State which parasite is depicted.
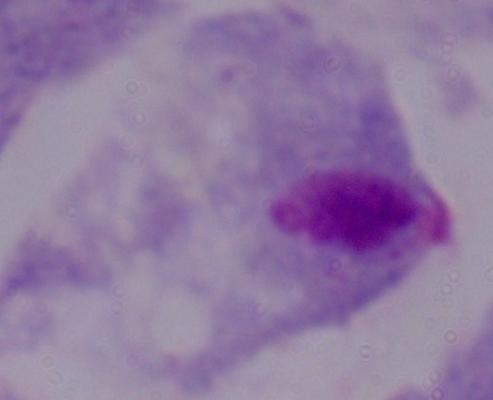

A trichomonad.

1000x magnification. Photomicrograph.